Locate every Plasmodium falciparum-infected red blood cell.
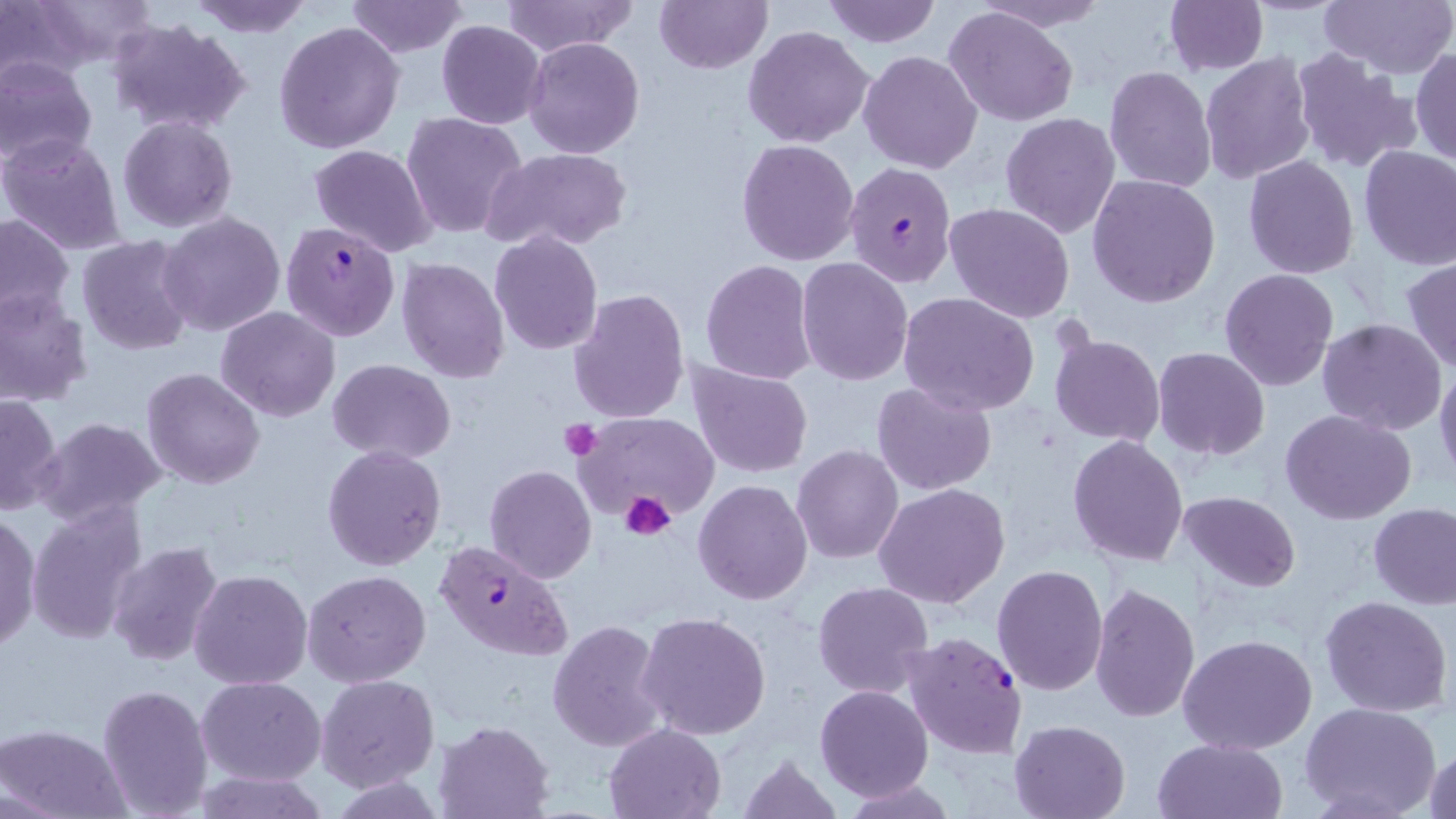

Approximate bounding boxes as [x1, y1, x2, y2] in pixels.
Plasmodium falciparum-infected red blood cells: [845, 160, 956, 287], [280, 222, 399, 340], [432, 539, 573, 661], [899, 632, 1028, 759].

Summary:
  - Platelet locations: [559, 420, 601, 460], [619, 490, 677, 541]
  - Uninfected red blood cell locations: [21, 0, 155, 71], [185, 0, 314, 36], [345, 0, 469, 57], [500, 0, 637, 56], [654, 0, 772, 73], [821, 0, 942, 48], [1318, 0, 1456, 81], [0, 1, 87, 88], [971, 1, 1113, 31], [1162, 1, 1268, 75], [941, 6, 1081, 129], [105, 17, 252, 135], [436, 20, 547, 130], [273, 21, 405, 155], [742, 25, 875, 149], [522, 37, 646, 158], [1410, 47, 1455, 165], [1289, 48, 1421, 175], [858, 50, 982, 173], [1199, 54, 1315, 184], [0, 59, 97, 169], [1104, 65, 1216, 193], [401, 113, 530, 241], [1000, 113, 1120, 239], [117, 116, 238, 234], [1, 133, 126, 255], [735, 139, 859, 266], [309, 144, 436, 257], [1358, 146, 1456, 270], [486, 147, 631, 255], [1243, 156, 1360, 279], [1087, 174, 1220, 307], [944, 202, 1076, 323], [158, 211, 287, 337], [0, 212, 75, 328], [488, 231, 604, 355], [76, 236, 197, 355], [396, 257, 512, 383], [1402, 257, 1456, 374], [796, 258, 915, 387], [700, 260, 817, 385], [1220, 267, 1339, 391], [0, 288, 94, 407], [569, 289, 690, 426], [898, 292, 1039, 415], [216, 307, 341, 422], [1316, 319, 1447, 435], [1047, 331, 1166, 446], [1152, 346, 1270, 459], [687, 358, 814, 479], [327, 359, 456, 463], [1434, 366, 1456, 485], [141, 368, 265, 490], [871, 380, 999, 494], [0, 392, 63, 517], [1280, 408, 1415, 525], [574, 410, 723, 529], [34, 417, 168, 527], [1068, 435, 1189, 565], [322, 444, 448, 572], [792, 445, 905, 565], [484, 464, 596, 583], [693, 480, 813, 604], [874, 484, 1010, 609], [1178, 491, 1301, 594], [27, 501, 147, 646], [1369, 504, 1456, 608], [0, 513, 40, 653], [106, 540, 226, 668], [991, 565, 1108, 696], [303, 569, 432, 687], [189, 570, 313, 690], [813, 582, 935, 699], [1088, 583, 1200, 724], [1321, 594, 1453, 718], [637, 610, 771, 741], [547, 620, 667, 751], [1178, 636, 1316, 755], [314, 674, 438, 793], [197, 676, 325, 785], [98, 684, 213, 817], [814, 684, 934, 802], [1300, 701, 1442, 819], [433, 719, 555, 818], [1010, 719, 1129, 818], [603, 722, 728, 818], [0, 723, 130, 819], [1152, 737, 1287, 819], [1425, 746, 1456, 819], [737, 754, 842, 819], [189, 770, 329, 819], [843, 779, 958, 819]
  - Slide-level diagnosis: Plasmodium falciparum
  - Stain: May-Grünwald-Giemsa
  - Field of view: one of a larger specimen
  - Magnification: 1000x
  - Image size: 1456×819 pixels
  - Modality: light microscopy
  - Preparation: thin blood smear